Give the position of every leukocyte visible.
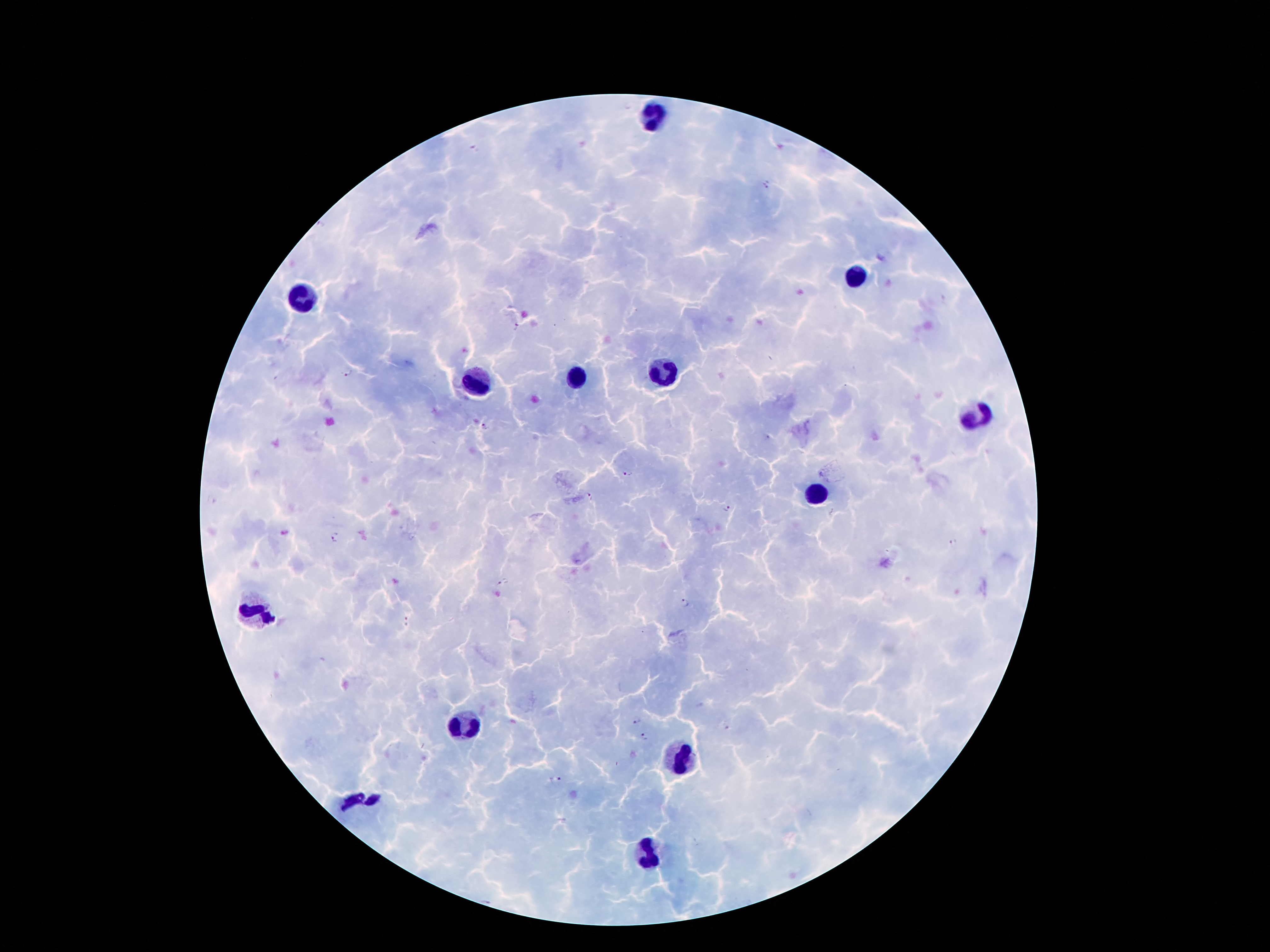

Approximate object centers, in pixels from the top-left corner.
Leukocytes: (x=651, y=116), (x=854, y=279), (x=306, y=300), (x=665, y=374), (x=577, y=380), (x=472, y=388), (x=976, y=414), (x=817, y=496), (x=256, y=611), (x=462, y=727), (x=682, y=758), (x=363, y=798), (x=649, y=851).

Plasmodium parasite locations = (x=474, y=150), (x=767, y=186), (x=514, y=328), (x=347, y=373), (x=483, y=427), (x=627, y=473), (x=589, y=496), (x=727, y=508), (x=335, y=538), (x=953, y=542), (x=503, y=583), (x=683, y=604), (x=407, y=622), (x=635, y=721), (x=644, y=737), (x=556, y=779)
capture = smartphone through the microscope eyepiece
preparation = thick peripheral-blood smear
patient malaria status = positive for Plasmodium falciparum
stain = Giemsa
magnification = 100x
image size = 1270×952 pixels
field of view = one from this slide